Locate every blood parasite and identify its species.
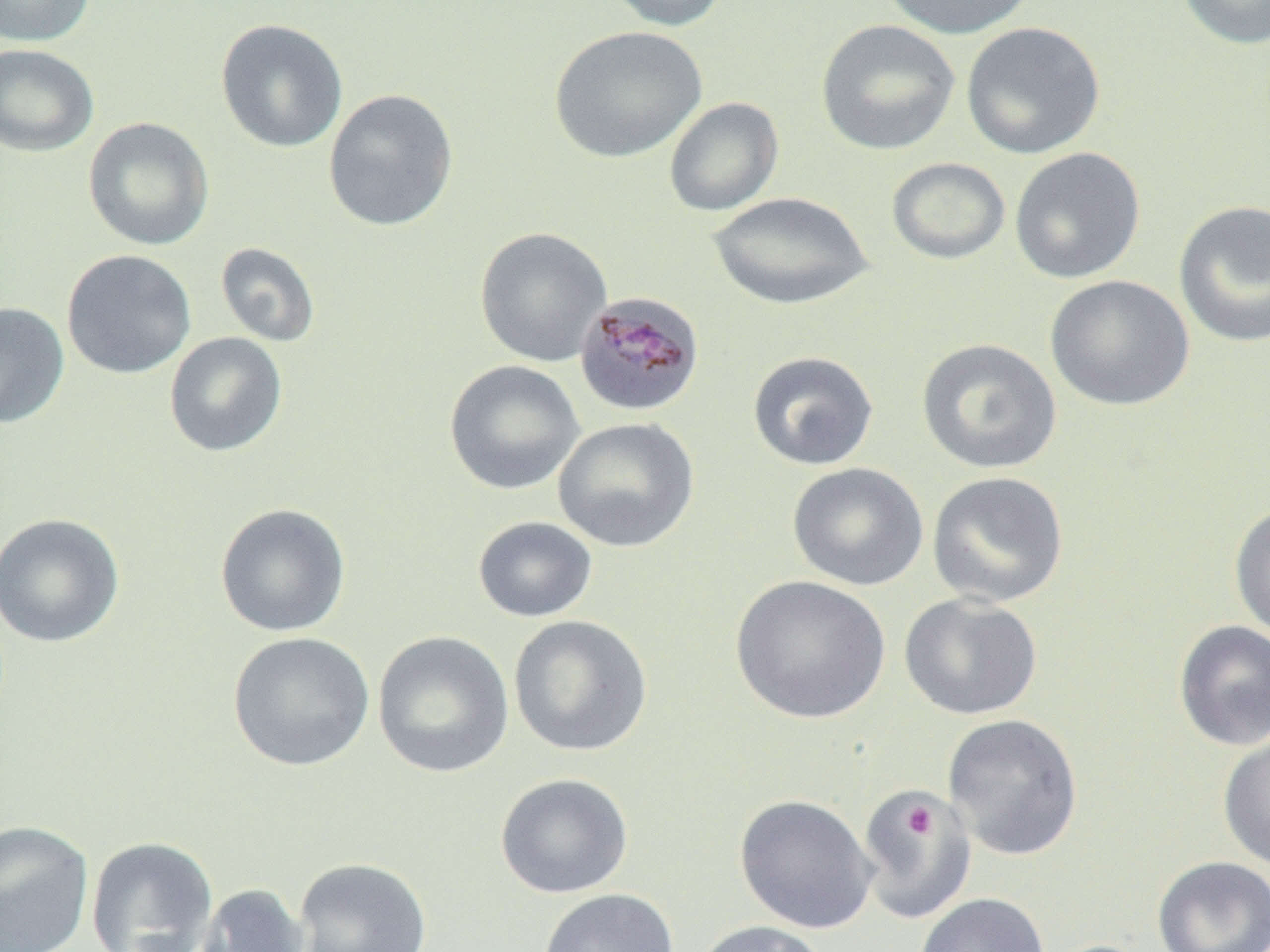

Approximate bounding boxes as [x1, y1, x2, y2] in pixels.
Plasmodium malariae-infected red blood cells: [573, 291, 706, 418].
No Plasmodium falciparum, Plasmodium ovale, Plasmodium vivax, Babesia divergens, or Trypanosoma brucei observed.

Summary:
  - Uninfected red blood cell locations: [0, 0, 97, 47], [601, 0, 730, 32], [877, 0, 1038, 40], [1177, 0, 1270, 50], [215, 18, 348, 153], [816, 19, 961, 156], [960, 21, 1106, 160], [549, 25, 707, 163], [0, 43, 99, 157], [323, 88, 459, 232], [663, 97, 784, 217], [82, 117, 215, 251], [1009, 146, 1146, 284], [886, 157, 1010, 265], [708, 191, 874, 311], [1173, 199, 1270, 349], [474, 227, 612, 367], [215, 242, 321, 348], [61, 249, 196, 379], [1044, 275, 1195, 411], [0, 302, 69, 428], [164, 332, 288, 457], [916, 337, 1062, 475], [747, 350, 879, 471], [444, 360, 585, 495], [552, 417, 700, 552], [787, 462, 928, 591], [926, 471, 1070, 609], [1228, 501, 1270, 642], [215, 502, 351, 637], [0, 512, 125, 648], [473, 516, 597, 623], [730, 574, 891, 724], [899, 593, 1043, 720], [508, 615, 653, 757], [1172, 620, 1270, 751], [372, 630, 515, 778], [227, 631, 375, 772], [941, 713, 1084, 862], [1217, 731, 1270, 871], [494, 772, 634, 898], [856, 787, 977, 923], [734, 794, 878, 934], [0, 820, 94, 952], [86, 836, 219, 951], [1152, 855, 1270, 952], [293, 856, 433, 951], [196, 883, 310, 952], [538, 888, 678, 952], [914, 892, 1049, 952], [694, 920, 828, 952]
  - Platelet locations: [902, 805, 938, 838]
  - Slide-level diagnosis: Plasmodium malariae
  - Preparation: thin blood film
  - Image size: 1270×952 pixels
  - Magnification: 1000x
  - Modality: light microscopy
  - Field of view: one of a larger specimen